Classify this cell by malaria status.
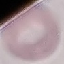

It is uninfected.

Cell patch, automatically extracted from a larger field of view and resized to 64 × 64 pixels. Giemsa stain. Acquired by smartphone through the microscope eyepiece. Thin blood film.